Describe the morphology of the erythrocytes.
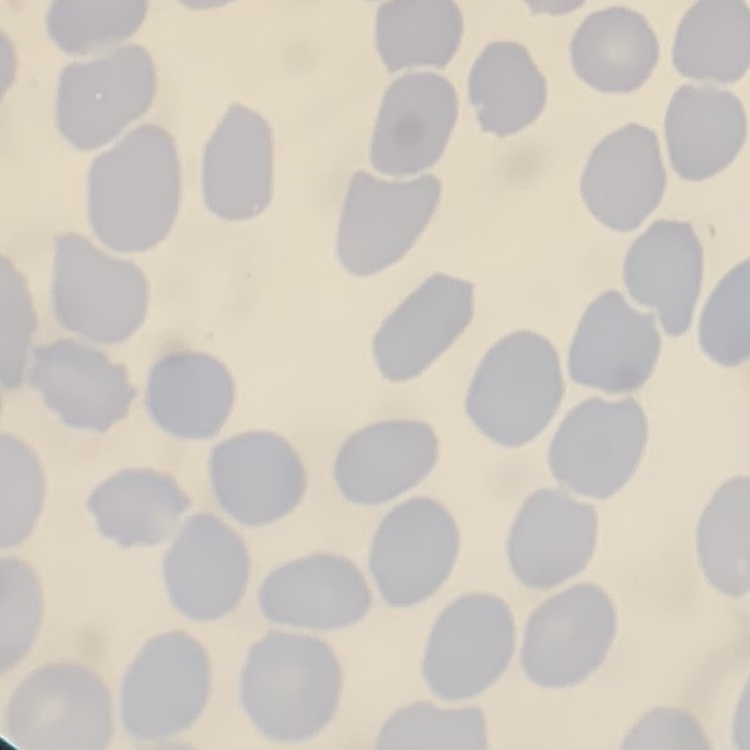

No rouleaux formation.

image_type: one tile cut from a larger photomicrograph
preparation: thin blood film
stain: Field's or Giemsa